Report the malaria status of this cell.
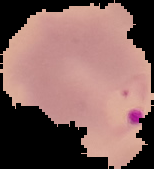
It is parasitized.

image size = 154×169 pixels
preparation = thin blood smear
image type = cell region segmented out of the field of view; surrounding area masked to black